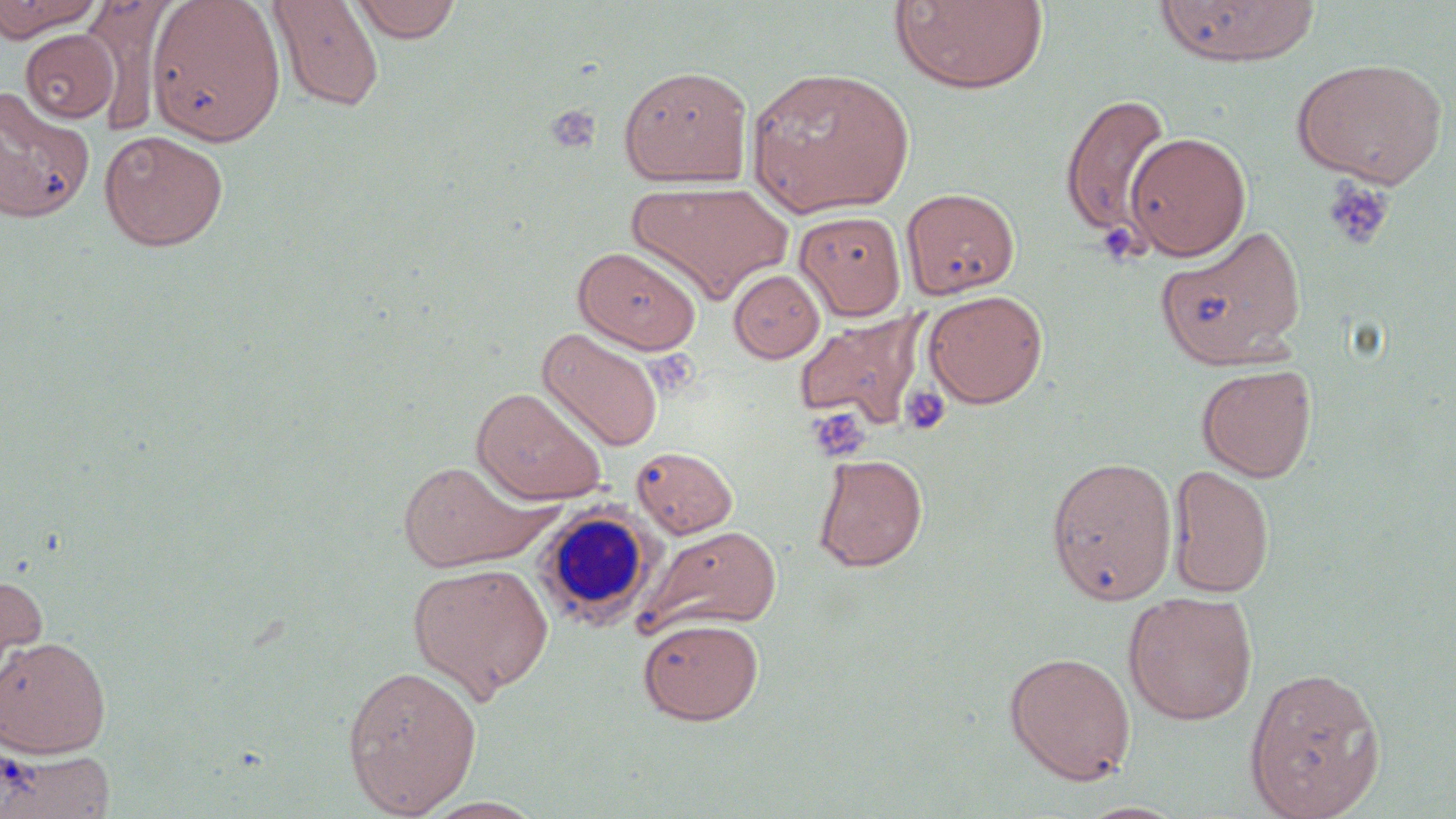 Approximate bounding boxes as named x1/y1/x2/y2 corners in pixels. Platelet locations: (x1=544, y1=104, x2=602, y2=156), (x1=1320, y1=177, x2=1394, y2=250), (x1=1095, y1=221, x2=1146, y2=266), (x1=900, y1=384, x2=951, y2=436), (x1=807, y1=408, x2=871, y2=462). White blood cell locations: (x1=534, y1=504, x2=658, y2=629). Uninfected red blood cell locations: (x1=0, y1=0, x2=102, y2=41), (x1=267, y1=0, x2=385, y2=113), (x1=350, y1=0, x2=462, y2=42), (x1=889, y1=0, x2=1049, y2=95), (x1=83, y1=1, x2=169, y2=135), (x1=146, y1=1, x2=285, y2=144), (x1=1153, y1=1, x2=1319, y2=67), (x1=19, y1=29, x2=119, y2=123), (x1=1292, y1=57, x2=1448, y2=187), (x1=618, y1=64, x2=753, y2=188), (x1=747, y1=65, x2=914, y2=218), (x1=0, y1=87, x2=95, y2=222), (x1=1060, y1=93, x2=1173, y2=238), (x1=99, y1=130, x2=229, y2=251), (x1=1125, y1=132, x2=1252, y2=261), (x1=627, y1=180, x2=794, y2=305), (x1=901, y1=187, x2=1020, y2=298), (x1=794, y1=211, x2=907, y2=320), (x1=1155, y1=225, x2=1307, y2=369), (x1=573, y1=246, x2=702, y2=354), (x1=729, y1=269, x2=825, y2=362), (x1=923, y1=289, x2=1048, y2=408), (x1=794, y1=312, x2=927, y2=427), (x1=538, y1=328, x2=663, y2=451), (x1=1196, y1=363, x2=1317, y2=482), (x1=472, y1=386, x2=607, y2=505), (x1=631, y1=445, x2=738, y2=539), (x1=812, y1=453, x2=928, y2=572), (x1=1046, y1=456, x2=1178, y2=605), (x1=397, y1=459, x2=549, y2=572), (x1=1168, y1=465, x2=1275, y2=598), (x1=637, y1=525, x2=781, y2=636), (x1=407, y1=561, x2=554, y2=700), (x1=0, y1=570, x2=48, y2=692), (x1=1123, y1=591, x2=1258, y2=725), (x1=638, y1=617, x2=764, y2=725), (x1=0, y1=635, x2=111, y2=758), (x1=1003, y1=651, x2=1137, y2=785), (x1=341, y1=664, x2=482, y2=817), (x1=1243, y1=665, x2=1386, y2=819), (x1=0, y1=747, x2=116, y2=818), (x1=417, y1=796, x2=548, y2=818). Slide-level diagnosis: negative for blood parasites. 1000x magnification. Light microscopy. One field of a larger specimen. May-Grünwald-Giemsa stain. Image is 1456×819 pixels. Thin blood smear.